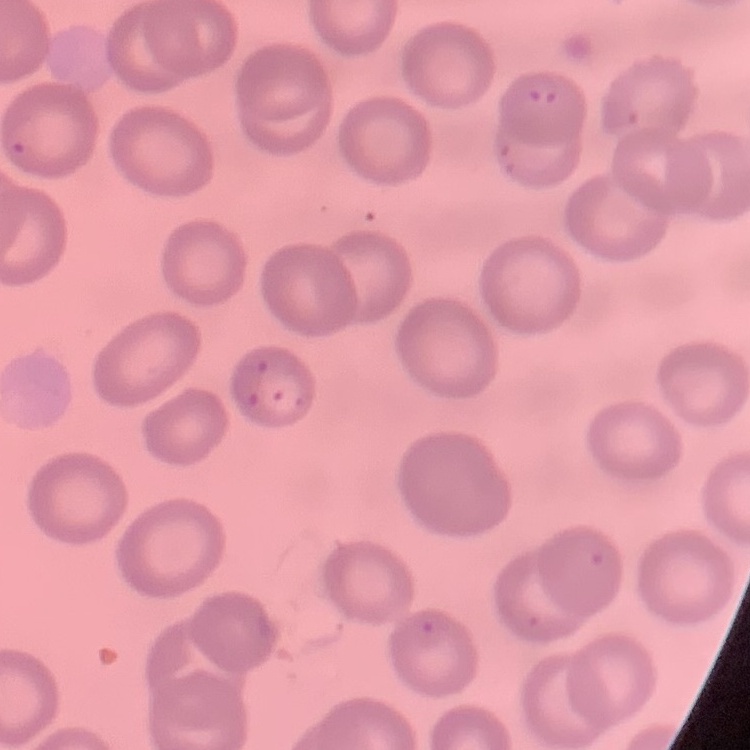
Summary:
  - Erythrocyte morphology: no rouleaux formation
  - Stain: Field's or Giemsa
  - Image type: square crop of a larger photomicrograph
  - Preparation: thin blood smear